Outline each Plasmodium ovale-infected red blood cell.
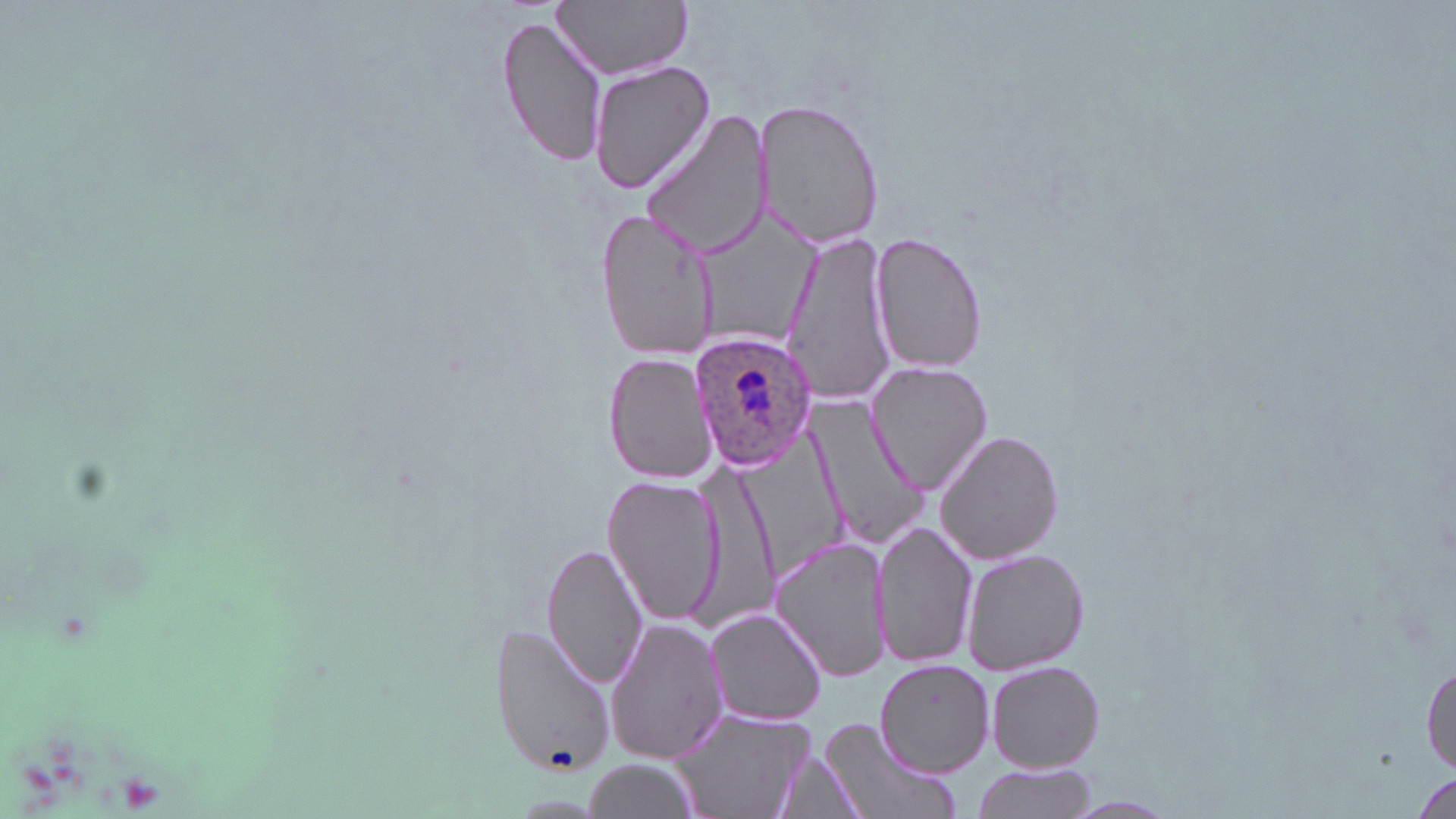
Approximate bounding boxes as (x1,y1)-(x2,y2) corner pairs in pixels.
Plasmodium ovale-infected red blood cells: (690,328)-(819,469).

{
  "slide_level_diagnosis": "Plasmodium ovale",
  "image_size": "1456×819 pixels",
  "preparation": "thin blood smear",
  "uninfected_red_blood_cell_locations": "approximate bounding boxes as (x1,y1)-(x2,y2) corner pairs in pixels: (552,0)-(693,80), (496,11)-(609,171), (586,60)-(717,197), (756,98)-(883,251), (638,109)-(775,261), (596,207)-(720,363), (869,231)-(989,375), (780,233)-(899,408), (604,352)-(719,483), (865,360)-(992,497), (802,394)-(928,555), (936,427)-(1064,565), (688,460)-(779,629), (603,475)-(725,626), (873,520)-(977,672), (770,535)-(891,683), (541,540)-(646,693), (962,549)-(1091,677), (703,608)-(828,726), (602,617)-(727,766), (490,624)-(615,777), (1419,654)-(1455,781), (874,658)-(996,778), (986,659)-(1106,772), (671,707)-(811,819), (817,719)-(958,819), (771,749)-(868,818), (584,759)-(697,816), (967,762)-(1099,819)",
  "modality": "optical microscopy",
  "field_of_view": "single",
  "magnification": "1000x",
  "stain": "May-Grünwald-Giemsa"
}